Outline each blood parasite and name the species.
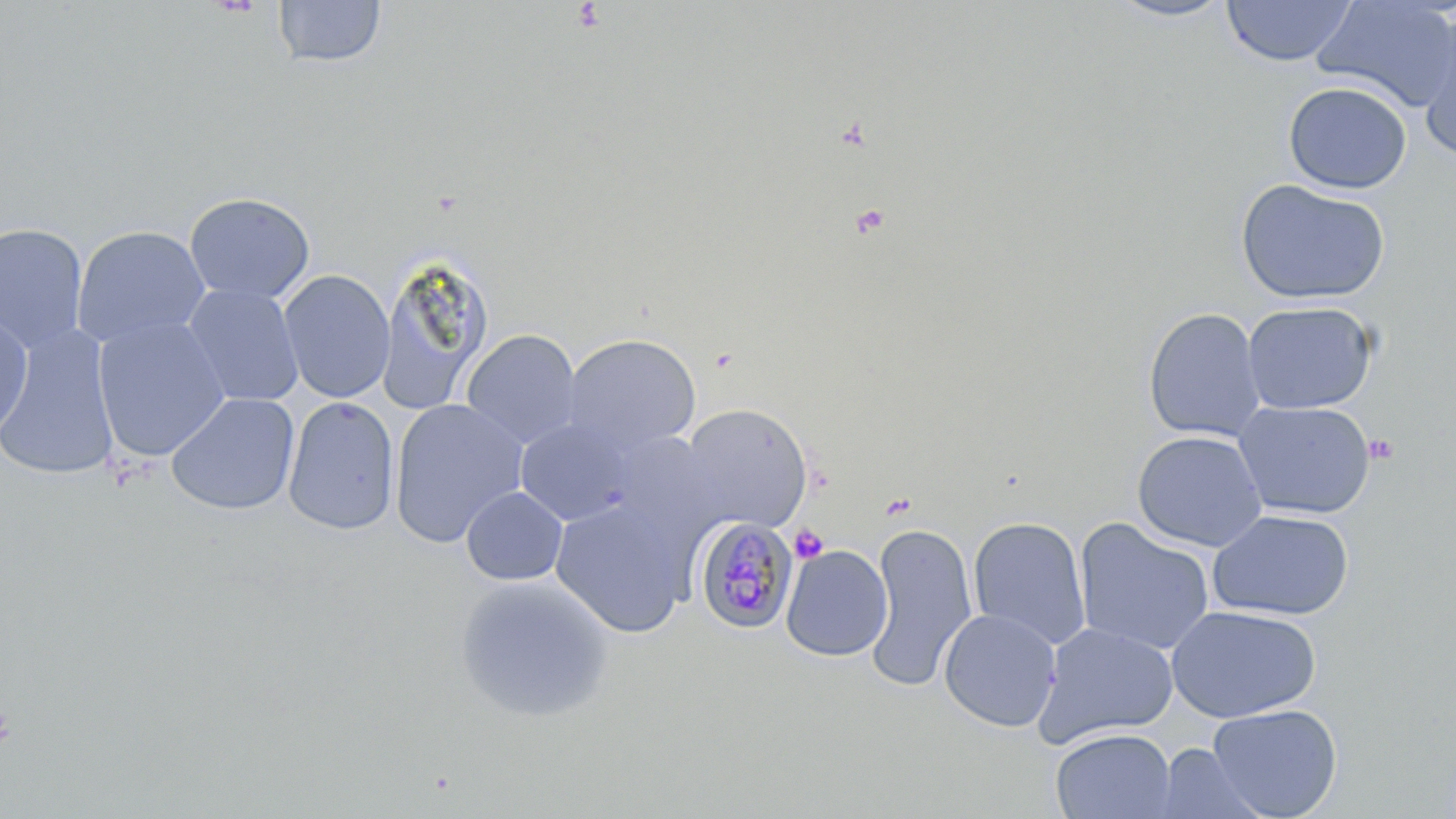

Approximate bounding boxes as (x1, y1, x2, y2) in pixels.
Plasmodium malariae-infected red blood cells: (692, 515, 799, 635).
No Plasmodium falciparum, Plasmodium ovale, Plasmodium vivax, Babesia divergens, or Trypanosoma brucei observed.

slide_level_diagnosis: Plasmodium malariae
uninfected_red_blood_cell_locations: 'approximate bounding boxes as (x1, y1, x2, y2) in pixels: (1221, 0, 1357, 67), (1311, 0, 1456, 111), (273, 1, 387, 68), (1105, 1, 1236, 23), (1416, 13, 1456, 158), (1283, 81, 1412, 194), (1234, 178, 1391, 306), (183, 192, 315, 305), (0, 222, 89, 352), (72, 225, 210, 349), (377, 252, 494, 414), (278, 269, 395, 404), (182, 283, 304, 407), (1241, 301, 1378, 415), (1142, 306, 1267, 443), (0, 310, 33, 440), (92, 316, 230, 461), (0, 326, 120, 483), (461, 329, 582, 448), (563, 333, 701, 455), (166, 392, 300, 516), (283, 396, 400, 537), (388, 398, 526, 548), (1233, 400, 1375, 520), (679, 403, 814, 533), (515, 418, 638, 526), (1131, 430, 1268, 552), (605, 433, 721, 537), (461, 486, 568, 586), (549, 499, 688, 638), (1207, 509, 1355, 621), (968, 516, 1091, 651), (1074, 517, 1216, 656), (864, 523, 978, 693), (780, 544, 893, 662), (455, 574, 615, 723), (1166, 604, 1321, 724), (938, 608, 1061, 733), (1033, 622, 1179, 748), (1207, 703, 1343, 819), (1050, 728, 1176, 819), (1153, 742, 1268, 819)'
preparation: thin blood film
stain: May-Grünwald-Giemsa
platelet_locations: 'approximate bounding boxes as (x1, y1, x2, y2) in pixels: (850, 203, 890, 238), (1364, 433, 1399, 465), (789, 524, 829, 564)'
modality: optical microscopy
image_size: 1456×819 pixels
field_of_view: single
magnification: 1000x